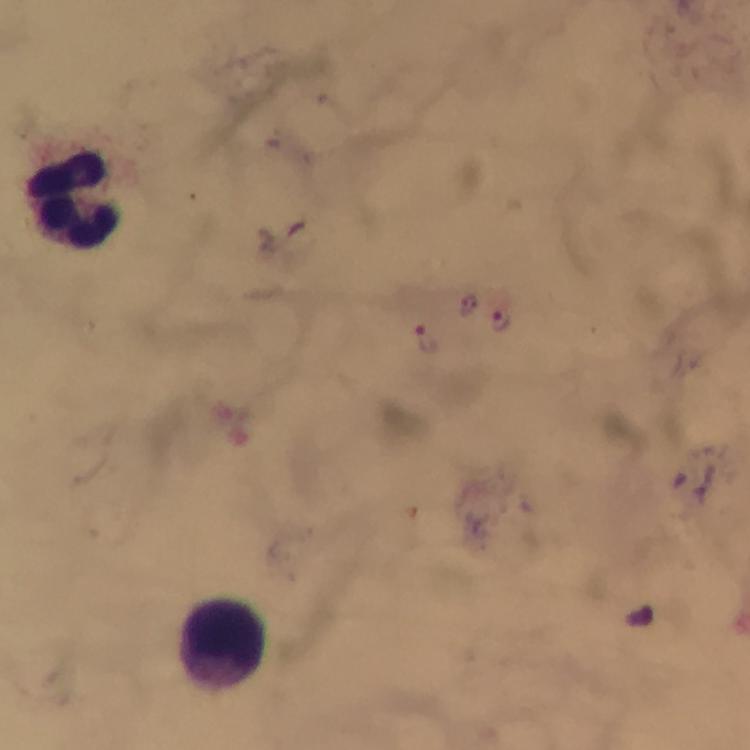
Approximate centers as (x, y) in pixels.
Summary:
  - Plasmodium parasite locations: (499, 320), (427, 339)
  - Leukocyte locations: (71, 201), (222, 641)
  - Preparation: thick blood film
  - Capture: smartphone photograph through a microscope
  - Cropped from: one field of view
  - Magnification: 100x
  - Stain: Giemsa
  - Image size: 750×750 pixels
  - Context: from a malaria diagnostic workup
  - Immersion oil: used